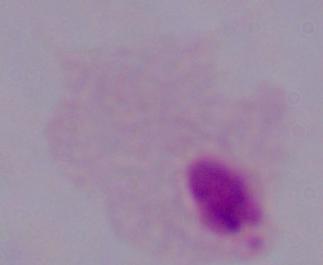

modality = micrograph
identification = trichomonad
magnification = 1000x